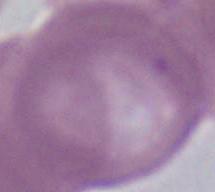
Summary:
  - Magnification: 1000x
  - Modality: photomicrograph
  - Identification: erythrocyte